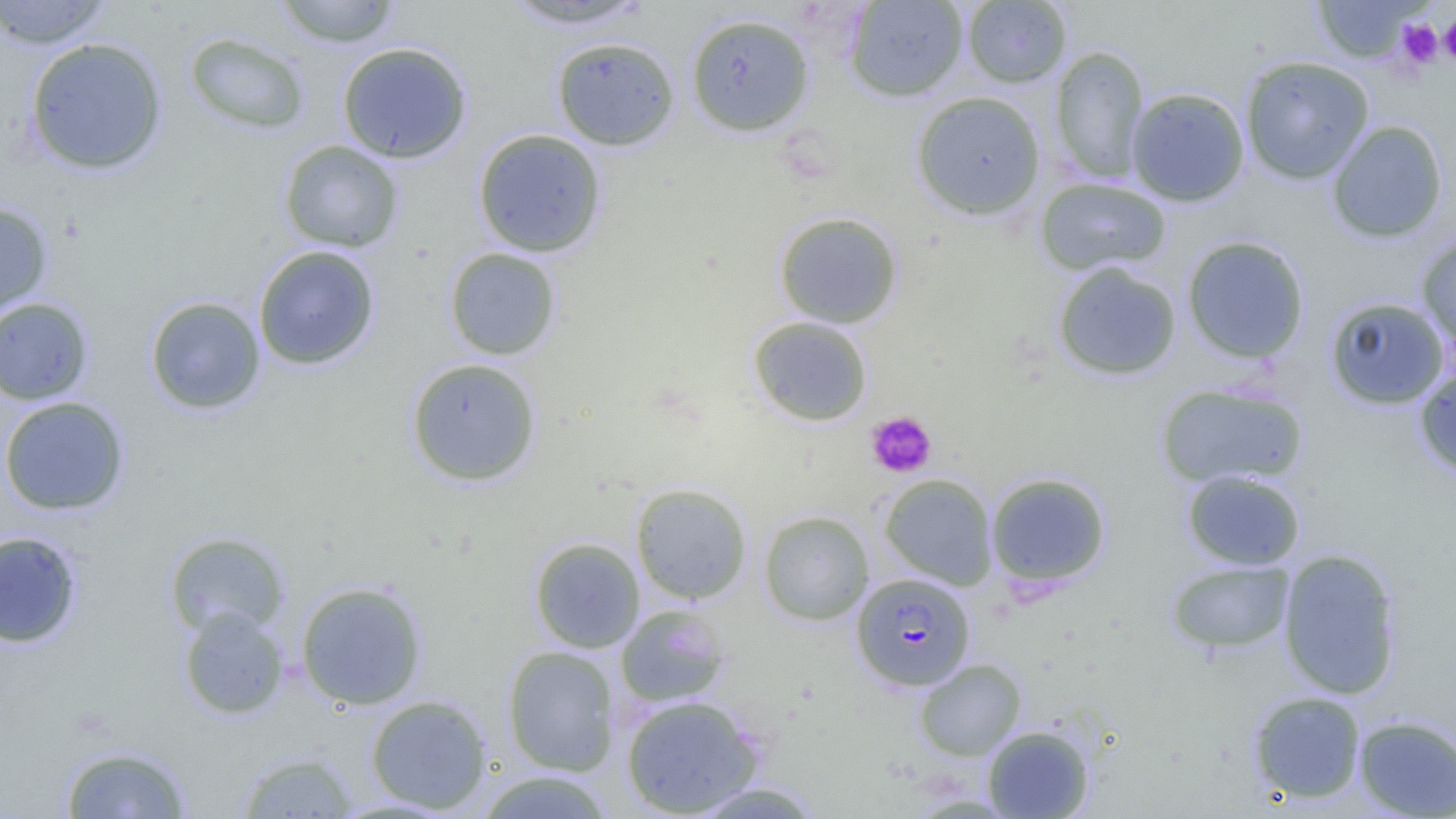

slide-level diagnosis = Plasmodium falciparum
modality = light microscopy
uninfected red blood cell locations = approximate bounding boxes as named x1/y1/x2/y2 corners in pixels: (x1=0, y1=0, x2=114, y2=49), (x1=273, y1=0, x2=402, y2=47), (x1=500, y1=0, x2=653, y2=30), (x1=1310, y1=0, x2=1426, y2=63), (x1=845, y1=1, x2=968, y2=102), (x1=962, y1=1, x2=1072, y2=88), (x1=685, y1=12, x2=815, y2=137), (x1=184, y1=32, x2=311, y2=135), (x1=24, y1=37, x2=168, y2=176), (x1=551, y1=37, x2=680, y2=151), (x1=336, y1=41, x2=472, y2=163), (x1=1049, y1=45, x2=1150, y2=184), (x1=1240, y1=55, x2=1375, y2=184), (x1=1126, y1=87, x2=1250, y2=206), (x1=910, y1=91, x2=1046, y2=221), (x1=1327, y1=120, x2=1449, y2=243), (x1=472, y1=128, x2=607, y2=258), (x1=278, y1=140, x2=405, y2=254), (x1=1035, y1=177, x2=1172, y2=276), (x1=0, y1=200, x2=53, y2=319), (x1=774, y1=211, x2=903, y2=329), (x1=1416, y1=234, x2=1456, y2=351), (x1=1181, y1=235, x2=1311, y2=365), (x1=253, y1=245, x2=380, y2=370), (x1=444, y1=247, x2=562, y2=361), (x1=1052, y1=261, x2=1182, y2=380), (x1=144, y1=296, x2=266, y2=415), (x1=1324, y1=296, x2=1451, y2=409), (x1=0, y1=297, x2=94, y2=405), (x1=747, y1=316, x2=874, y2=426), (x1=405, y1=357, x2=542, y2=486), (x1=1413, y1=366, x2=1456, y2=480), (x1=1154, y1=381, x2=1309, y2=489), (x1=0, y1=396, x2=130, y2=516), (x1=1181, y1=468, x2=1306, y2=571), (x1=985, y1=472, x2=1112, y2=588), (x1=879, y1=473, x2=998, y2=590), (x1=631, y1=482, x2=752, y2=604), (x1=759, y1=509, x2=874, y2=625), (x1=0, y1=530, x2=83, y2=649), (x1=164, y1=530, x2=290, y2=638), (x1=529, y1=537, x2=645, y2=653), (x1=1277, y1=547, x2=1403, y2=700), (x1=1166, y1=559, x2=1295, y2=655), (x1=295, y1=580, x2=428, y2=710), (x1=615, y1=605, x2=730, y2=708), (x1=177, y1=606, x2=290, y2=720), (x1=502, y1=645, x2=620, y2=775), (x1=914, y1=658, x2=1026, y2=761), (x1=1247, y1=690, x2=1367, y2=805), (x1=365, y1=694, x2=493, y2=814), (x1=620, y1=695, x2=764, y2=817), (x1=1354, y1=715, x2=1455, y2=818), (x1=982, y1=725, x2=1095, y2=818), (x1=58, y1=743, x2=194, y2=818), (x1=236, y1=751, x2=359, y2=818), (x1=472, y1=770, x2=618, y2=818), (x1=686, y1=780, x2=827, y2=818)
Plasmodium falciparum-infected red blood cell locations = approximate bounding boxes as named x1/y1/x2/y2 corners in pixels: (x1=852, y1=573, x2=975, y2=690)
platelet locations = approximate bounding boxes as named x1/y1/x2/y2 corners in pixels: (x1=1440, y1=14, x2=1456, y2=67), (x1=1396, y1=18, x2=1444, y2=69), (x1=866, y1=411, x2=936, y2=478)
field of view = one of a larger specimen
image size = 1456×819 pixels
magnification = 1000x
preparation = thin blood film